Give the preparation type.
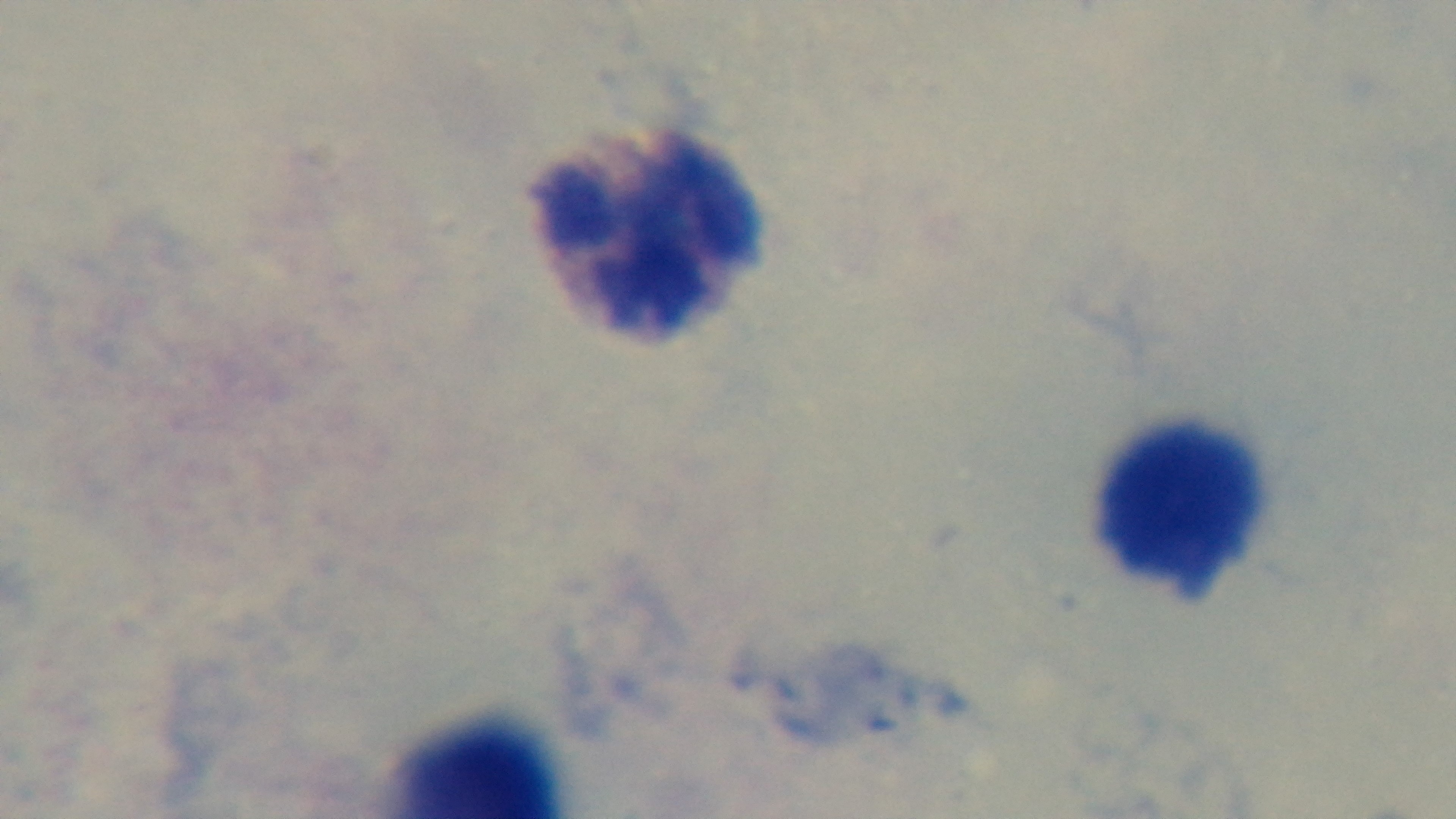
It is a thick blood film.

{
  "field_of_view": "single",
  "modality": "light microscopy",
  "objective": "100x oil immersion",
  "malaria_status": "uninfected",
  "stain": "Giemsa",
  "capture": "mounted 4K digital camera"
}